Assess this cell for malaria.
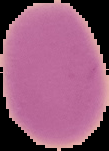

Uninfected.

Image is 109×151 pixels. Cell region segmented out of the field of view; the surrounding area is masked to black. From a thin blood smear.